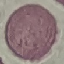
Summary:
  - Result: no malaria parasites seen
  - Image type: cell patch, automatically extracted from a larger field of view and resized to 64 × 64 pixels
  - Preparation: thin smear
  - Stain: Giemsa
  - Capture: smartphone camera at the microscope eyepiece